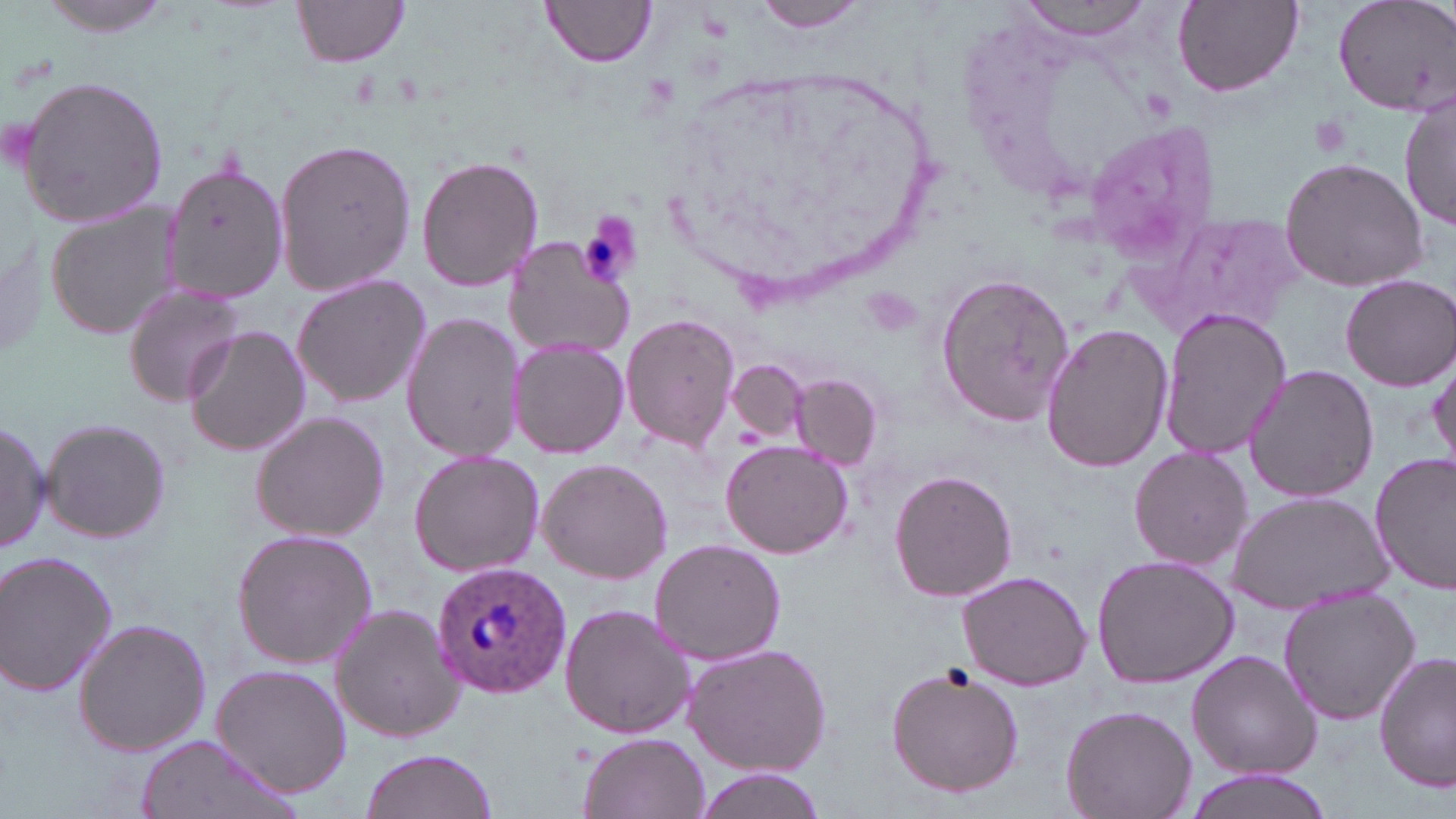
Approximate bounding boxes as (x1,y1)-(x2,y2) corner pairs in pixels. Plasmodium ovale-infected red blood cell locations: (431,559)-(569,697). Platelet locations: (1307,110)-(1358,159), (579,213)-(643,287). Uninfected red blood cell locations: (31,0)-(185,37), (292,0)-(412,69), (754,0)-(876,35), (1015,0)-(1156,41), (1172,0)-(1303,97), (1331,0)-(1456,116), (542,1)-(655,69), (15,75)-(171,227), (1401,90)-(1455,237), (1082,118)-(1219,260), (272,138)-(416,298), (417,155)-(544,291), (1279,156)-(1431,289), (163,158)-(287,307), (46,204)-(185,341), (1143,212)-(1301,340), (502,234)-(634,359), (936,268)-(1075,430), (1338,272)-(1456,389), (290,273)-(431,409), (120,281)-(250,407), (1158,308)-(1289,462), (400,311)-(525,462), (620,314)-(741,453), (1039,322)-(1174,474), (183,324)-(309,458), (508,335)-(630,460), (1430,349)-(1456,470), (727,359)-(807,443), (1242,364)-(1380,503), (792,373)-(881,469), (248,410)-(390,543), (40,416)-(171,543), (0,417)-(50,558), (721,440)-(853,559), (1127,445)-(1253,571), (407,451)-(545,578), (1371,453)-(1456,593), (536,457)-(673,584), (889,469)-(1018,604), (1228,490)-(1395,612), (231,528)-(378,669), (648,538)-(786,667), (0,549)-(119,697), (1090,554)-(1241,689), (957,569)-(1095,690), (1277,586)-(1425,726), (329,602)-(466,742), (559,604)-(697,739), (72,617)-(212,758), (683,641)-(834,777), (1187,649)-(1321,780), (1374,651)-(1455,793), (884,661)-(1026,797), (211,662)-(354,798), (1061,704)-(1196,819), (578,731)-(708,819), (131,734)-(303,819), (359,748)-(497,819), (688,768)-(822,818), (1176,769)-(1340,819). Slide-level diagnosis: Plasmodium ovale. 1000x magnification. One field of a larger specimen. Thin blood film. Image is 1456×819 pixels. Optical microscopy. May-Grünwald-Giemsa-stained preparation.